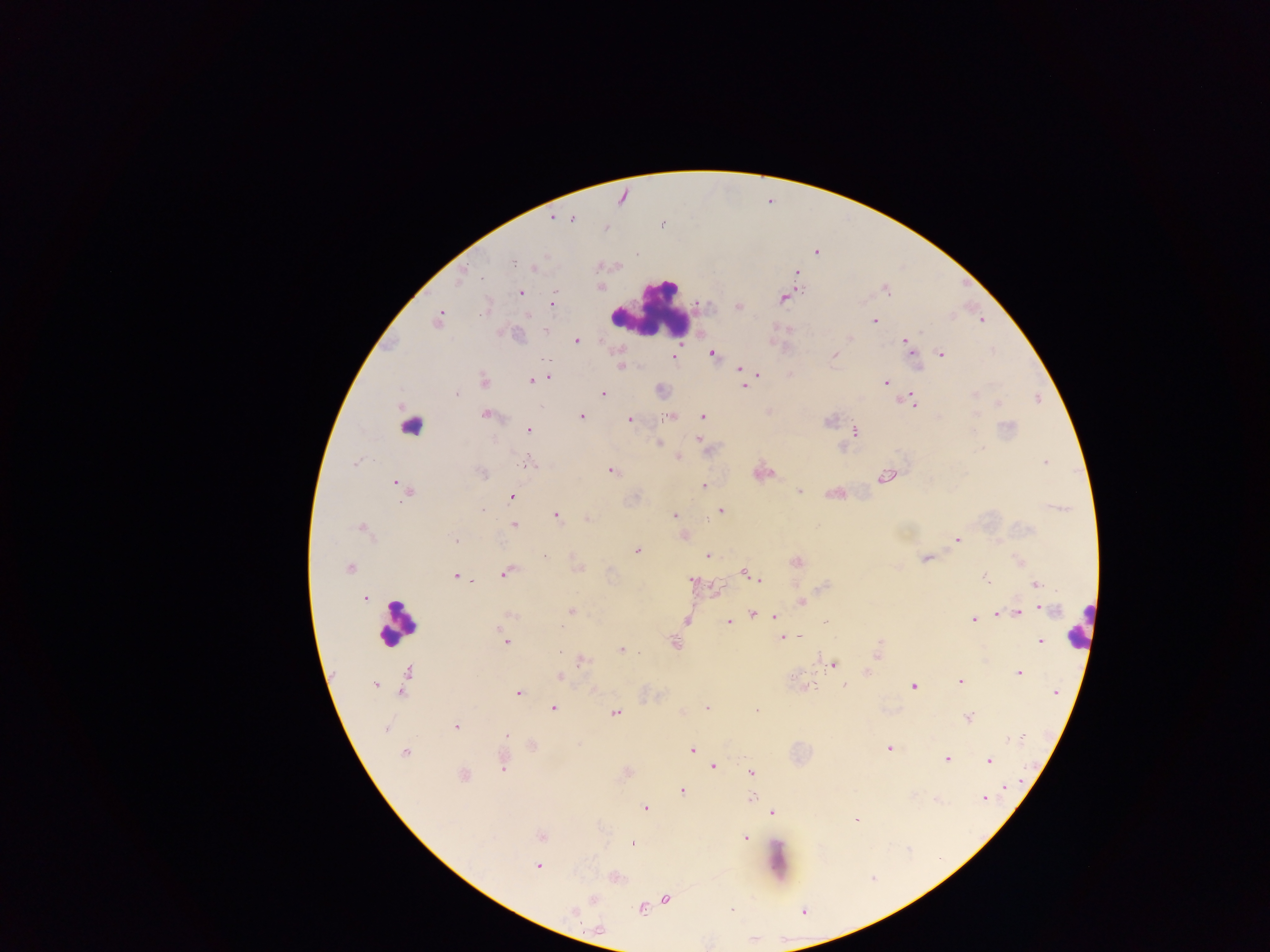

country: Ghana
capture: mobile-phone photograph through a microscope
preparation: thick blood film
field_of_view: single
malaria_parasite_locations: 'approximate centers as [x, y] in pixels: [553, 218], [571, 219], [606, 228], [637, 253], [512, 261], [535, 268], [797, 272], [482, 277], [461, 278], [886, 290], [520, 293], [783, 299], [553, 302], [737, 307], [528, 316], [439, 319], [982, 320], [874, 321], [849, 339], [576, 341], [906, 343], [910, 348], [942, 353], [712, 354], [835, 355], [674, 357], [622, 366], [740, 369], [757, 375], [549, 377], [532, 380], [484, 381], [741, 382], [886, 383], [744, 386], [602, 393], [975, 394], [456, 395], [912, 400], [998, 403], [485, 414], [977, 414], [670, 416], [702, 416], [581, 417], [630, 420], [828, 420], [528, 430], [855, 431], [698, 439], [658, 443], [982, 449], [679, 458], [1045, 462], [530, 463], [355, 464], [611, 471], [482, 472], [886, 477], [397, 483], [507, 485], [704, 486], [407, 491], [799, 492], [721, 510], [482, 511], [675, 515], [556, 516], [587, 519], [513, 525], [362, 528], [455, 540], [958, 540], [636, 550], [544, 556], [708, 556], [925, 558], [796, 562], [349, 569], [505, 573], [746, 573], [455, 577], [985, 578], [759, 579], [692, 581], [1036, 585], [365, 598], [802, 602], [1045, 610], [571, 611], [753, 612], [1018, 612], [998, 613], [774, 616], [974, 619], [686, 620], [728, 622], [826, 622], [561, 626], [800, 636], [783, 638], [1040, 641], [506, 642], [675, 642], [559, 651], [621, 651], [878, 651], [583, 660], [832, 664], [407, 672], [1019, 673], [559, 677], [960, 682], [375, 684], [810, 686], [845, 686], [914, 687], [401, 692], [519, 692], [1055, 692], [553, 708], [707, 708], [756, 712], [615, 713], [968, 717], [455, 727], [385, 728], [506, 736], [1019, 737], [1012, 739], [533, 745], [890, 748], [692, 750], [404, 752], [947, 759], [989, 761], [713, 766], [502, 767], [752, 772], [464, 775], [1008, 787], [682, 791], [752, 798], [984, 800], [645, 809], [773, 812], [856, 820], [542, 836], [745, 838], [633, 844], [537, 866], [594, 899], [666, 899], [641, 909], [732, 909], [574, 912]'
leukocyte_locations: 'approximate centers as [x, y] in pixels: [649, 310], [413, 424], [397, 622], [1079, 625]'
image_size: 1270×952 pixels